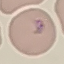

Result: malaria parasites identified. Thin blood film. Cell patch, automatically extracted from a larger field of view and resized to 64 × 64 pixels. Giemsa-stained preparation. Acquired by smartphone through the microscope eyepiece.